Assess this cell for malaria.
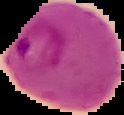
It is parasitized.

Summary:
  - Preparation: thin blood smear
  - Image type: segmented cell region with the area outside set to black
  - Image size: 124×115 pixels